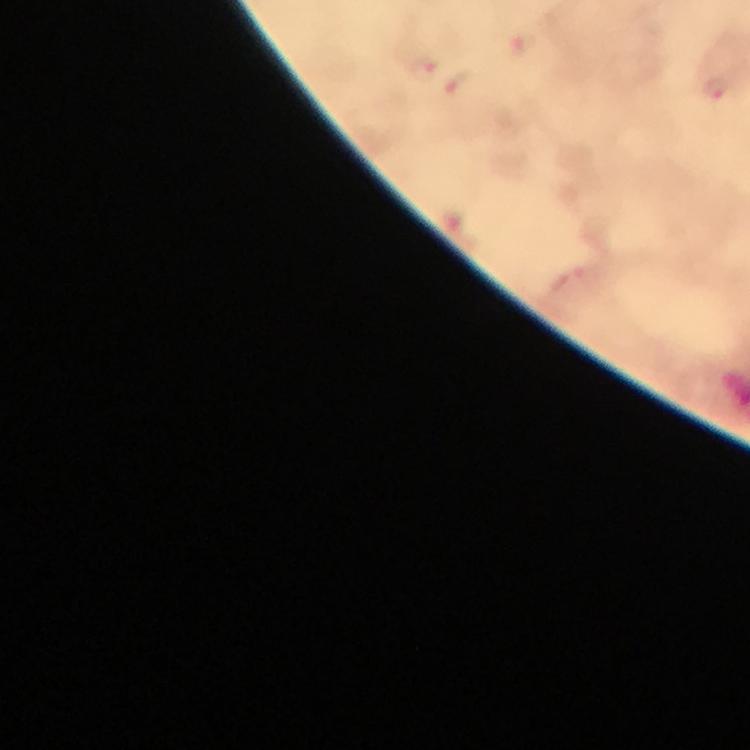

Approximate centers as [x, y] in pixels.
Summary:
  - Malaria parasite locations: [423, 65], [458, 83], [718, 88]
  - Cropped from: one field of view
  - Magnification: 100x
  - Stain: Giemsa
  - Context: from a diagnostic examination for malaria
  - Image size: 750×750 pixels
  - Immersion oil: applied
  - Capture: smartphone photograph through a microscope
  - Preparation: thick smear